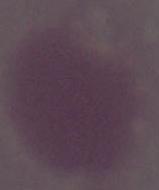
Summary:
  - Modality: micrograph
  - Magnification: 1000x
  - Identification: red blood cell